State the blood parasite species.
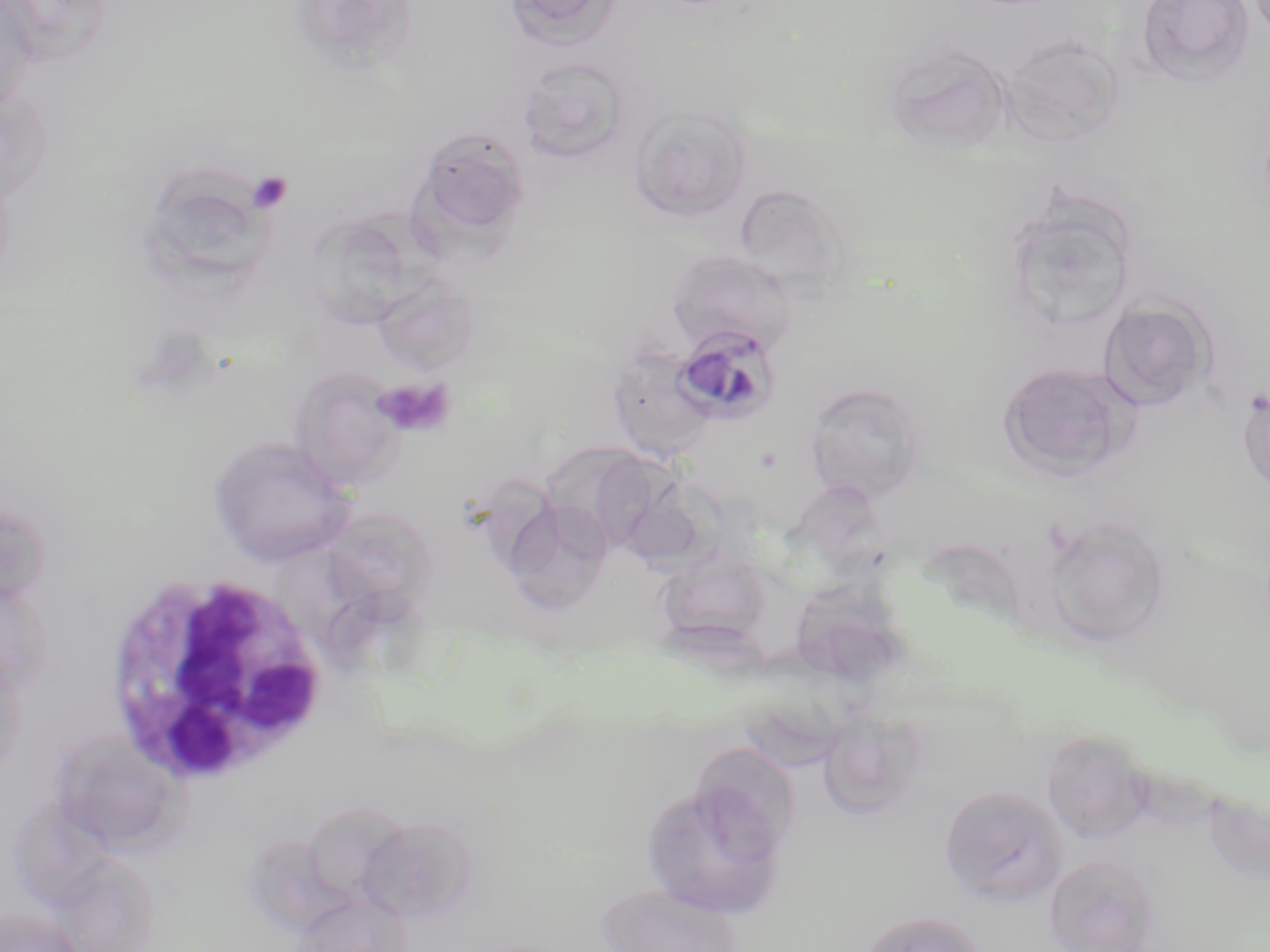

Plasmodium malariae.

Approximate bounding boxes as named x1/y1/x2/y2 corners in pixels. Plasmodium malariae-infected red blood cell locations: (x1=672, y1=325, x2=782, y2=426). Platelet locations: (x1=245, y1=170, x2=293, y2=214), (x1=373, y1=377, x2=455, y2=437). Uninfected red blood cell locations: (x1=0, y1=0, x2=38, y2=114), (x1=288, y1=0, x2=420, y2=74), (x1=1136, y1=0, x2=1255, y2=87), (x1=503, y1=1, x2=621, y2=50), (x1=0, y1=2, x2=66, y2=83), (x1=998, y1=33, x2=1125, y2=149), (x1=882, y1=42, x2=1012, y2=152), (x1=517, y1=57, x2=634, y2=165), (x1=0, y1=87, x2=51, y2=207), (x1=628, y1=105, x2=752, y2=224), (x1=411, y1=125, x2=532, y2=246), (x1=151, y1=169, x2=269, y2=283), (x1=734, y1=182, x2=850, y2=295), (x1=349, y1=195, x2=452, y2=302), (x1=1003, y1=197, x2=1138, y2=334), (x1=312, y1=212, x2=417, y2=330), (x1=666, y1=249, x2=796, y2=355), (x1=373, y1=274, x2=480, y2=376), (x1=1098, y1=298, x2=1214, y2=411), (x1=606, y1=346, x2=718, y2=462), (x1=998, y1=361, x2=1135, y2=479), (x1=289, y1=367, x2=406, y2=492), (x1=803, y1=381, x2=928, y2=503), (x1=1237, y1=381, x2=1270, y2=499), (x1=207, y1=435, x2=356, y2=568), (x1=540, y1=442, x2=663, y2=549), (x1=620, y1=477, x2=726, y2=572), (x1=503, y1=498, x2=615, y2=614), (x1=321, y1=506, x2=439, y2=623), (x1=1040, y1=516, x2=1171, y2=648), (x1=655, y1=550, x2=775, y2=652), (x1=798, y1=579, x2=918, y2=691), (x1=816, y1=707, x2=928, y2=822), (x1=48, y1=729, x2=187, y2=854), (x1=1042, y1=730, x2=1157, y2=844), (x1=698, y1=746, x2=813, y2=861), (x1=639, y1=775, x2=789, y2=919), (x1=940, y1=785, x2=1069, y2=908), (x1=354, y1=815, x2=478, y2=923), (x1=1044, y1=854, x2=1161, y2=952), (x1=596, y1=883, x2=746, y2=952), (x1=297, y1=890, x2=414, y2=952), (x1=0, y1=905, x2=83, y2=952), (x1=858, y1=911, x2=985, y2=952). White blood cell locations: (x1=104, y1=568, x2=332, y2=788). Thin blood smear. Light microscopy. Image is 1270×952 pixels. 1000x magnification. Single field of view. May-Grünwald-Giemsa stain.